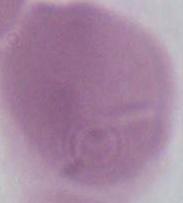
Captured at 1000x magnification. Micrograph. A red blood cell is shown.